Outline every leukocyte.
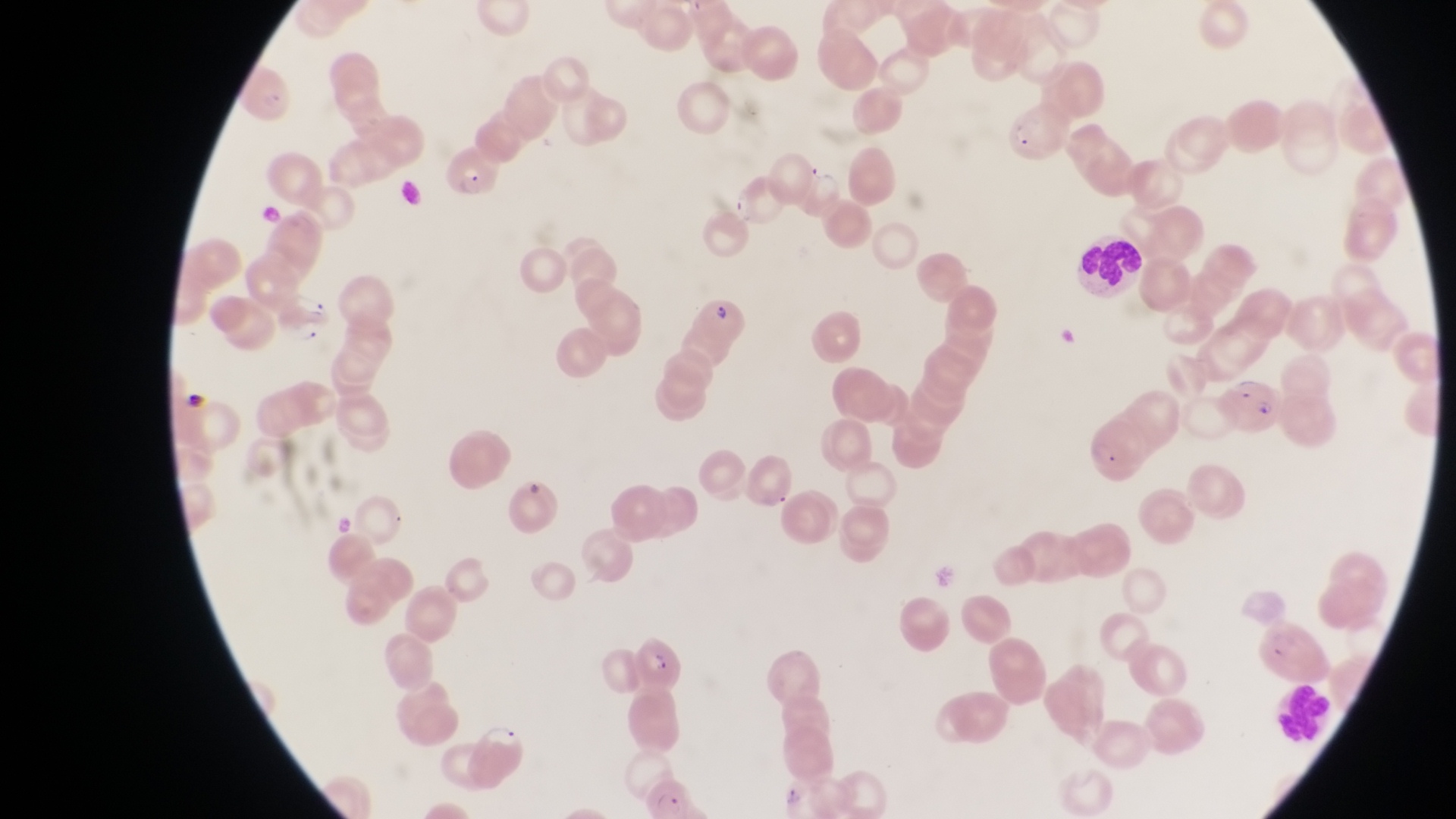

Approximate bounding boxes as (left, top, right, bottom) in pixels.
Leukocytes: (1072, 232, 1148, 296).

country = Uganda
image size = 1456×819 pixels
magnification = 1000x
preparation = thin blood film
capture = smartphone photograph through the eyepiece of an Olympus CX-23 microscope
field of view = single
parasitised red blood cell locations = approximate bounding boxes as (left, top, right, bottom) in pixels: (1003, 99, 1063, 162), (447, 148, 499, 201), (727, 177, 786, 232), (692, 294, 751, 344), (1226, 376, 1287, 431), (623, 634, 690, 692)